Describe the morphology of the erythrocytes.
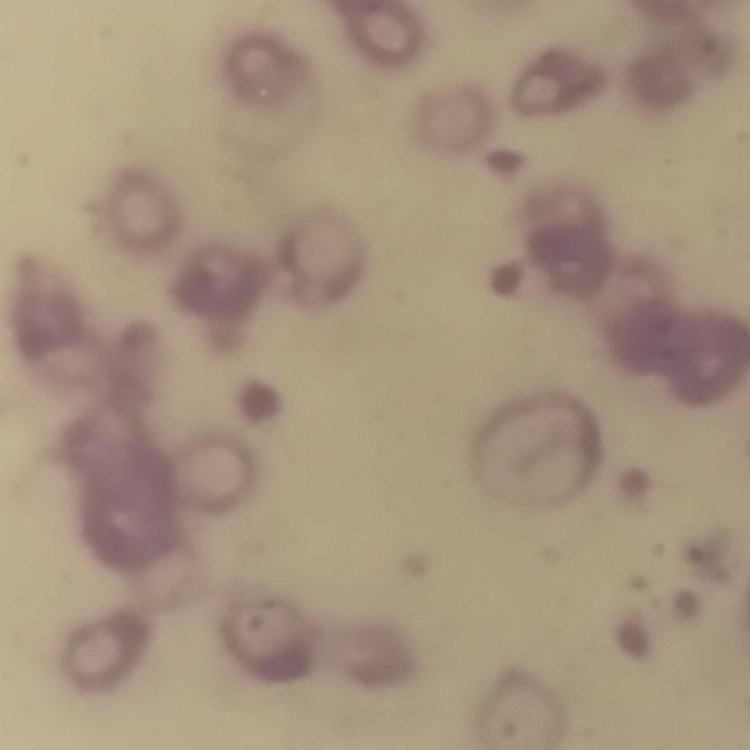

Rouleaux formation.

image type = one tile cut from a larger photomicrograph
stain = Field's or Giemsa
preparation = thin peripheral smear